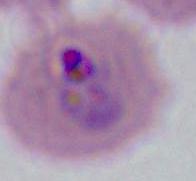

A Plasmodium parasite is shown. Photomicrograph. 400x or 1000x magnification.